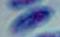

{
  "identification": "Toxoplasma gondii",
  "magnification": "1000x",
  "modality": "micrograph"
}